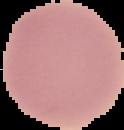

image type = segmented cell region on a black background
image size = 124×130 pixels
preparation = thin blood film
malaria status = uninfected